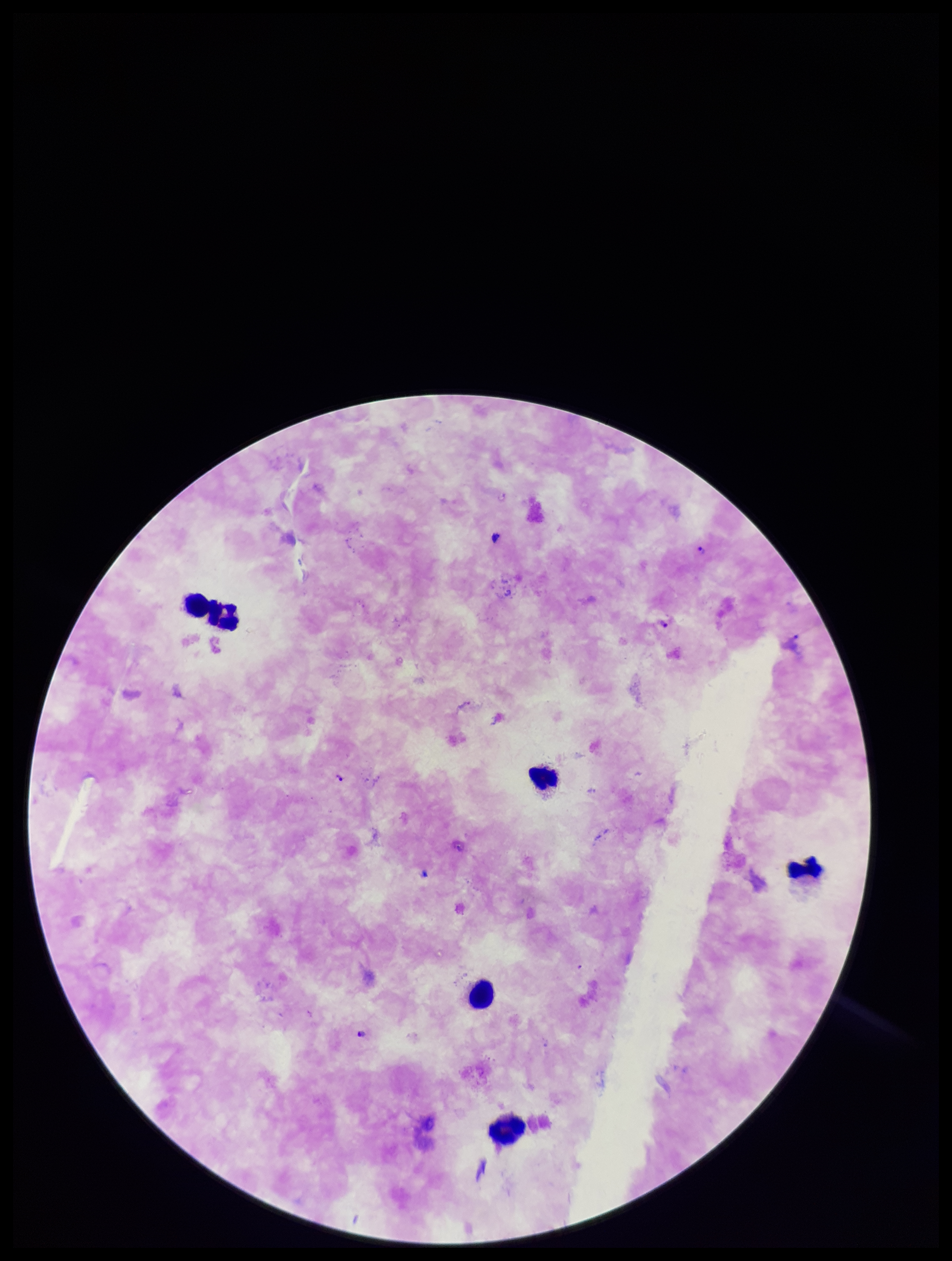
Plasmodium parasites = identified
field of view = single
preparation = thick
species reported for this patient = Plasmodium falciparum
parasite count = 4
leukocyte count = 6
stain = Giemsa
capture = smartphone photograph through the microscope eyepiece
patient malaria status = infected
image size = 952×1261 pixels